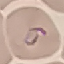
Result: malaria parasites identified. Thin smear of blood. Cell patch, automatically extracted from a larger field of view and resized to 64 × 64 pixels. Acquired by smartphone through the microscope eyepiece. Giemsa stain.